Give the position of every Plasmodium parasite visible.
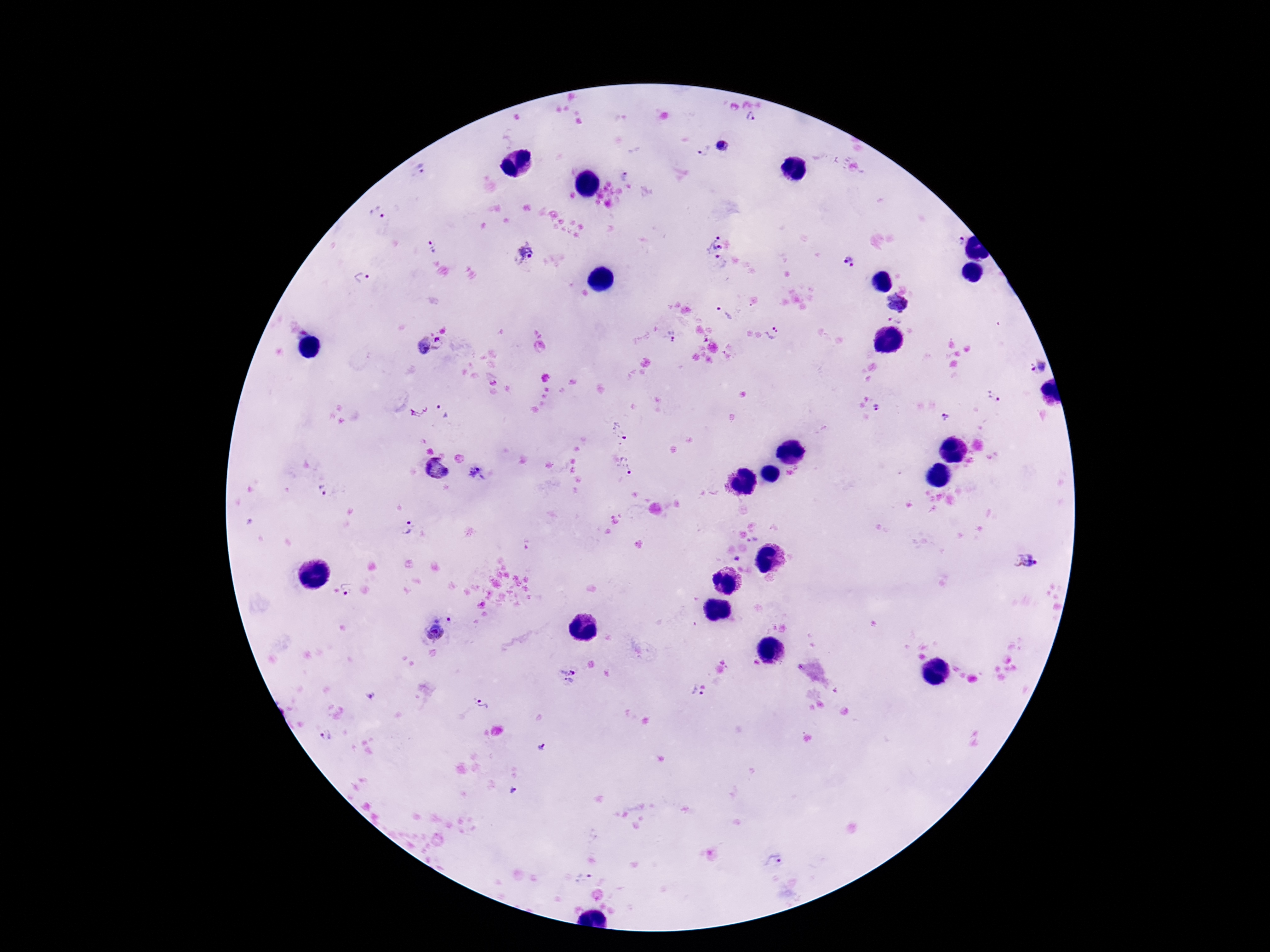
Approximate object centers, in pixels from the top-left corner.
Plasmodium parasites: (x=751, y=117), (x=722, y=146), (x=702, y=149), (x=421, y=168), (x=378, y=212), (x=714, y=238), (x=959, y=241), (x=432, y=247), (x=525, y=254), (x=719, y=262), (x=849, y=262), (x=360, y=278), (x=898, y=301), (x=724, y=314), (x=896, y=320), (x=773, y=333), (x=669, y=335), (x=439, y=343), (x=422, y=345), (x=1038, y=367), (x=993, y=395), (x=877, y=407), (x=442, y=409), (x=418, y=411), (x=945, y=416), (x=618, y=430), (x=625, y=467), (x=437, y=470), (x=477, y=472), (x=323, y=490), (x=406, y=528), (x=752, y=540), (x=737, y=558), (x=1026, y=560), (x=347, y=591), (x=442, y=610), (x=434, y=633), (x=568, y=664), (x=569, y=681), (x=370, y=694), (x=696, y=694), (x=483, y=703), (x=327, y=734), (x=541, y=748), (x=513, y=790), (x=773, y=861), (x=583, y=878).

stain = Giemsa
patient malaria status = infected
magnification = 100x
capture = smartphone camera through the microscope eyepiece
image size = 1270×952 pixels
preparation = thick blood film
field of view = single